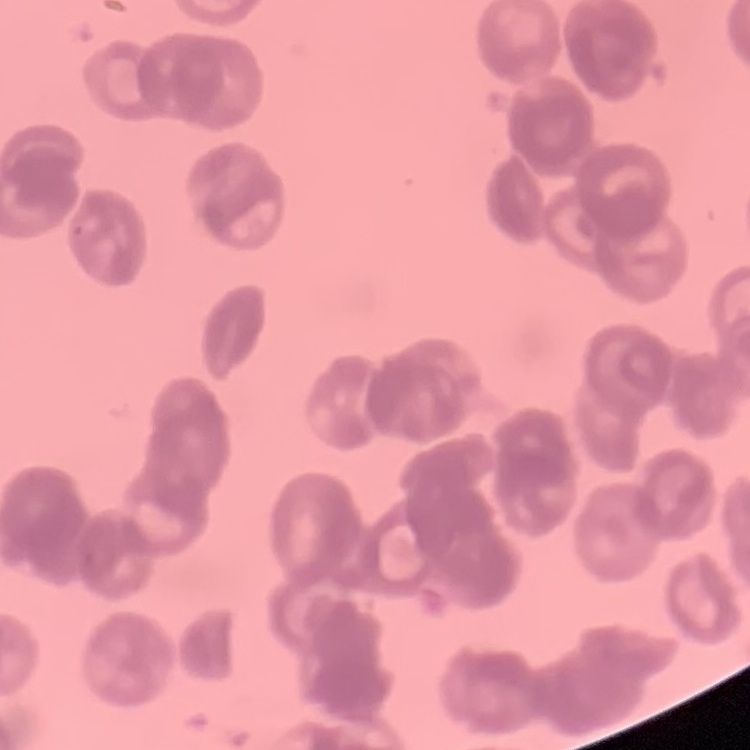

red blood cell morphology = rouleaux formation
stain = Field's or Giemsa
image type = square crop of a larger photomicrograph
preparation = thin blood smear